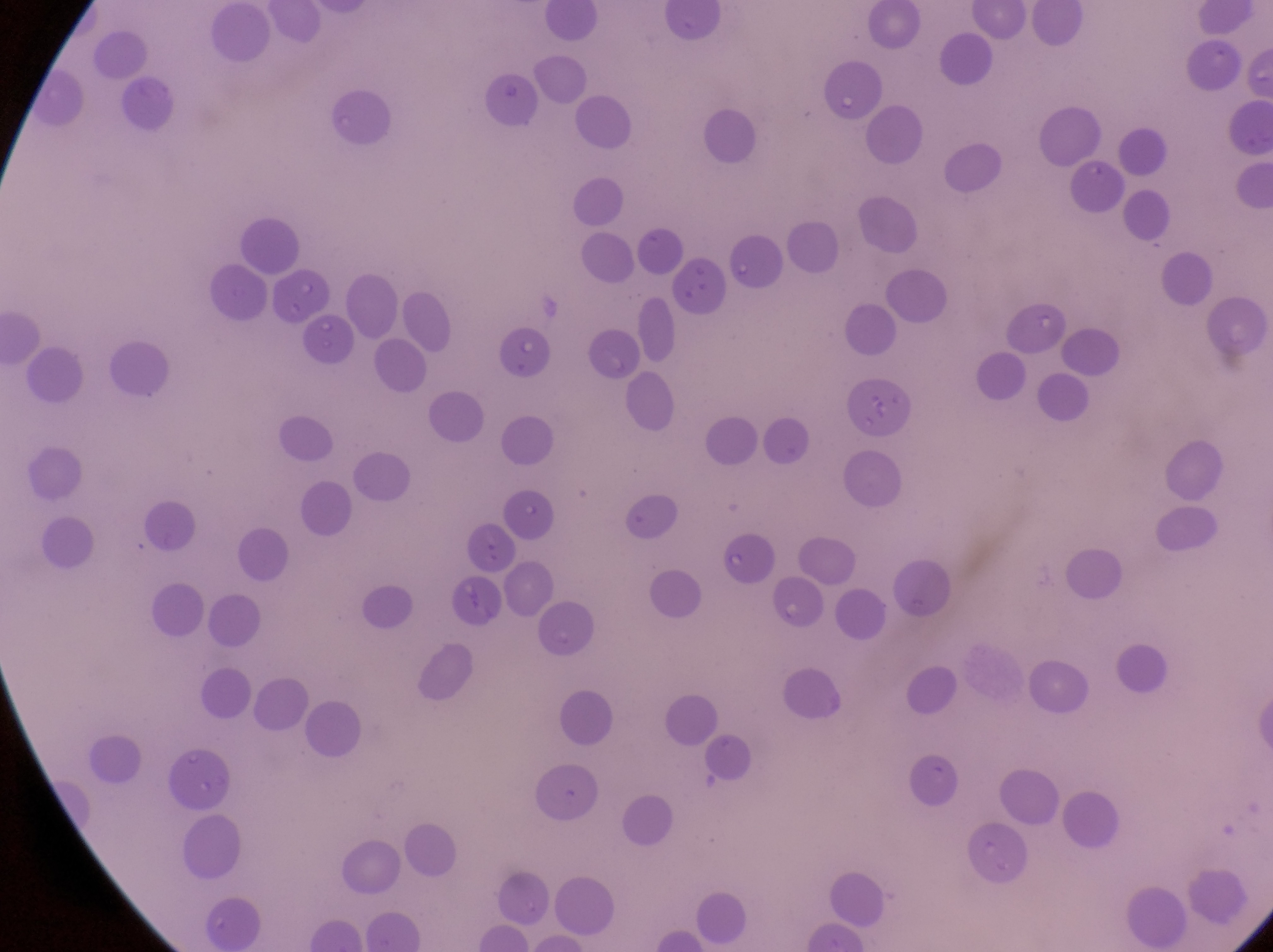
Approximate bounding boxes as (left, top, right, bottom) in pixels. Artifact (platelet-like body, stain precipitate, or debris) locations: (481, 74, 539, 129), (716, 240, 778, 293). Thin blood smear. At a magnification of 1000x. Captured by a smartphone held over the eyepiece of an Olympus CX-23 microscope. Sample from Uganda. One field of view. Image is 1273×952 pixels.